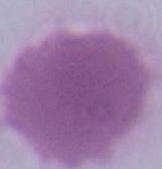

magnification = 1000x
identification = red blood cell
modality = photomicrograph